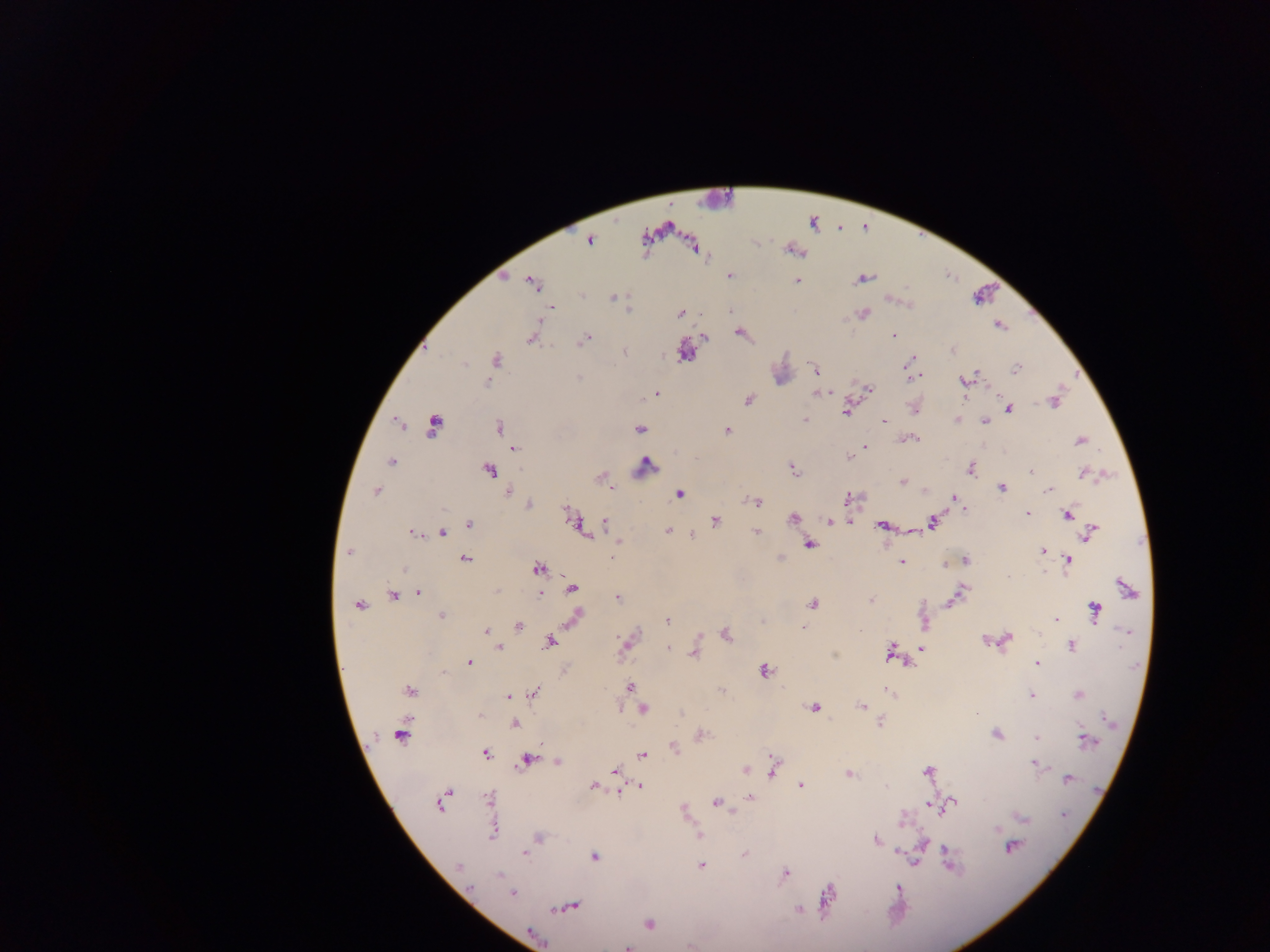

Approximate centers as x y in pixels.
Summary:
  - Leukocyte locations: 722 201; 987 297; 783 367; 899 914
  - Malaria parasite locations: 590 240; 729 276; 864 278; 797 280; 532 283; 614 297; 552 308; 628 310; 863 314; 680 315; 999 325; 740 334; 893 335; 704 337; 530 339; 585 340; 953 350; 685 352; 624 353; 496 359; 464 364; 910 364; 1017 369; 814 370; 913 376; 971 377; 579 378; 965 381; 487 382; 869 389; 656 394; 818 394; 824 394; 749 400; 1053 402; 915 409; 1009 409; 846 412; 804 420; 958 420; 883 421; 985 421; 433 426; 498 426; 639 429; 728 430; 911 439; 1080 441; 865 447; 515 449; 850 458; 392 461; 646 465; 793 468; 972 469; 489 471; 1030 471; 1085 473; 600 477; 902 482; 613 487; 1002 488; 1049 490; 376 491; 924 491; 508 492; 680 494; 849 498; 954 498; 757 501; 528 505; 1027 514; 1067 514; 793 518; 716 521; 933 521; 574 522; 832 522; 469 524; 605 524; 881 525; 668 531; 442 532; 756 532; 412 533; 1090 534; 692 535; 809 544; 1042 550; 348 553; 612 557; 465 560; 966 560; 1068 560; 902 561; 945 564; 538 569; 405 570; 1007 576; 572 588; 1127 588; 497 591; 418 592; 540 593; 958 595; 393 596; 618 597; 871 600; 813 604; 359 605; 1094 610; 441 616; 575 616; 1056 618; 667 621; 518 626; 803 628; 486 631; 1128 632; 1038 633; 726 635; 1007 640; 986 641; 550 642; 625 644; 1071 646; 921 647; 498 648; 669 649; 891 651; 695 653; 469 662; 1038 664; 765 670; 564 671; 443 673; 630 686; 410 690; 534 691; 889 692; 1078 694; 508 696; 1032 696; 812 707; 861 707; 643 709; 479 715; 515 724; 700 734; 997 734; 401 735; 1036 738; 1085 739; 673 747; 486 753; 642 755; 527 760; 558 762; 1037 764; 773 767; 615 770; 745 771; 928 772; 849 774; 1067 778; 593 786; 640 786; 801 786; 750 798; 488 799; 716 802; 952 804; 440 805; 934 805; 1064 816; 1022 818; 901 819; 493 832; 699 836; 538 837; 876 840; 924 843; 1011 847; 524 853; 744 854; 594 857; 913 860; 950 861; 701 865; 460 866; 785 873; 500 874; 898 888; 512 893; 828 898; 571 906; 799 910; 648 923; 534 935; 627 947
  - Preparation: thick blood smear
  - Capture: mobile-phone photograph through a microscope
  - Field of view: single
  - Country: Ghana
  - Image size: 1270×952 pixels